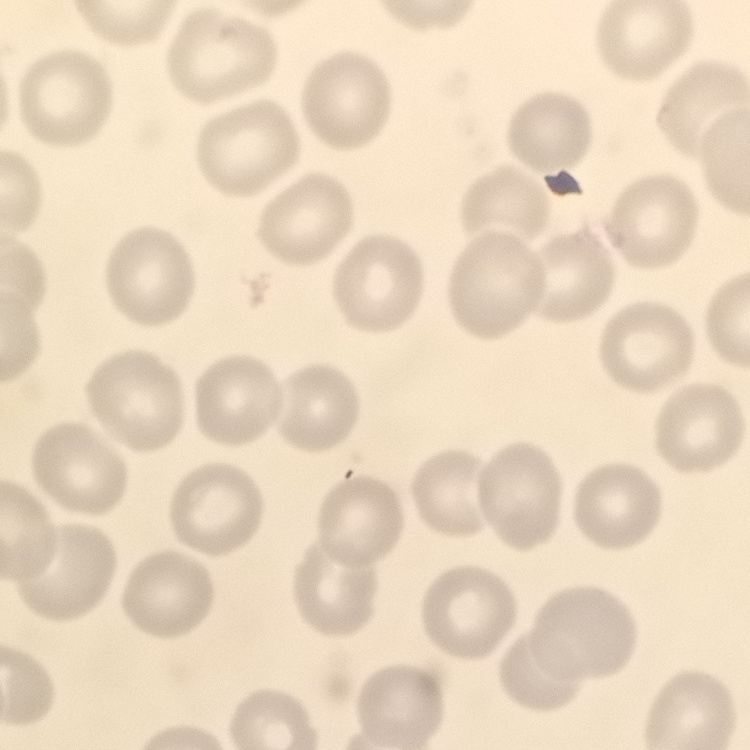
The erythrocytes show no rouleaux formation. Stained with either Field's or Giemsa. Thin blood smear. One tile cut from a larger photomicrograph.